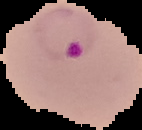 Segmented cell region on a black background. From a thin blood film. Result: Plasmodium parasites detected. Image is 142×130 pixels.